Identify the preparation type.
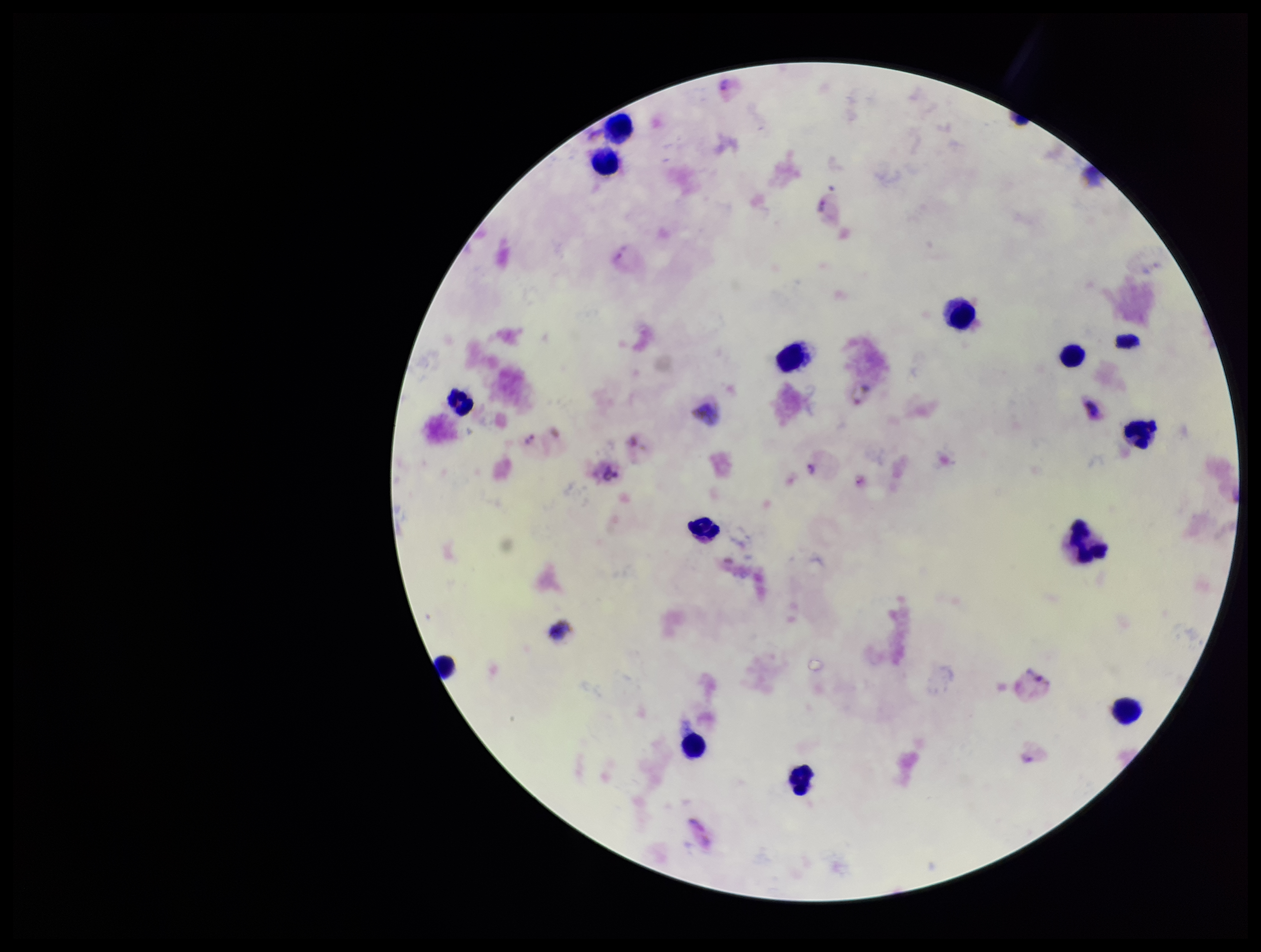
It is a thick blood smear.

parasite count = 5
capture = smartphone photograph through the microscope eyepiece
field of view = single
patient malaria status = positive
leukocyte count = 14
stain = Giemsa
Plasmodium parasites = detected
species reported for this patient = Plasmodium vivax
image size = 1261×952 pixels